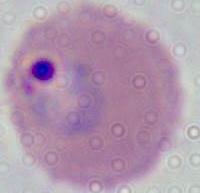
Micrograph. Captured at either 400x or 1000x magnification. A Plasmodium parasite is shown.